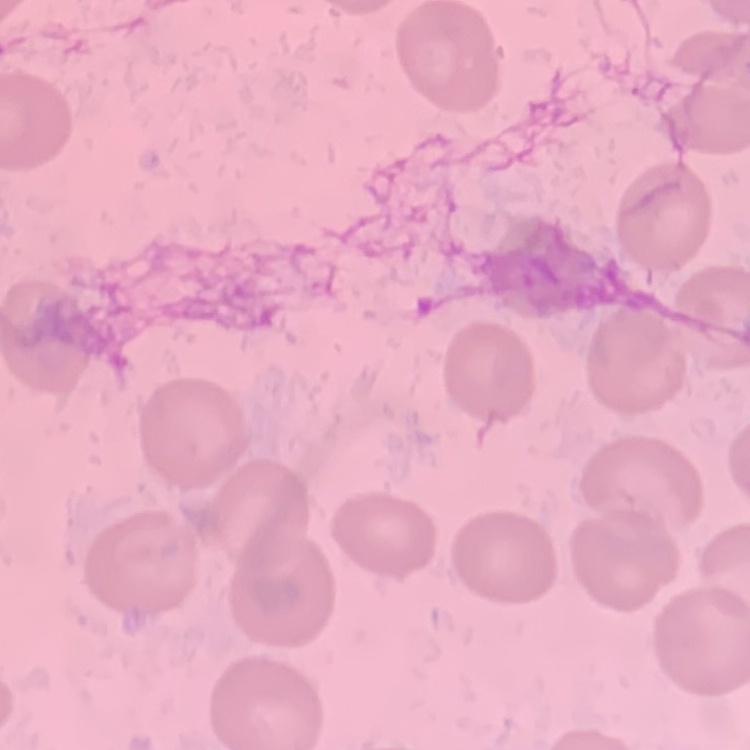

erythrocyte morphology = no rouleaux formation
image type = square crop of a larger photomicrograph
preparation = thin blood film
stain = Field's or Giemsa